Name the parasite shown.
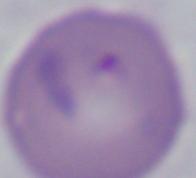
This is Babesia.

Captured at 1000x magnification. Micrograph.